Classify this cell by malaria status.
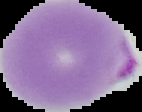

Parasitized.

image size = 142×112 pixels
preparation = thin blood smear
image type = segmented cell region with the area outside set to black